Assess this cell for malaria.
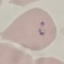

Parasitized.

Summary:
  - Preparation: thin smear
  - Stain: Giemsa
  - Image type: automatically extracted cell patch, resized to 64 × 64 pixels
  - Capture: smartphone through the microscope eyepiece